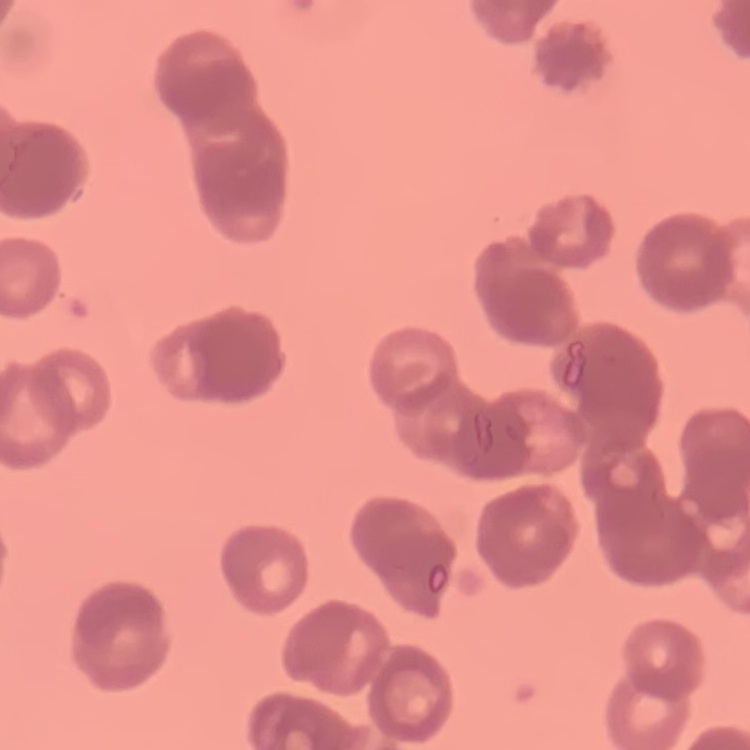
erythrocyte_morphology: rouleaux formation
stain: Field's or Giemsa
image_type: one tile cut from a larger photomicrograph
preparation: thin peripheral smear